Report the malaria status.
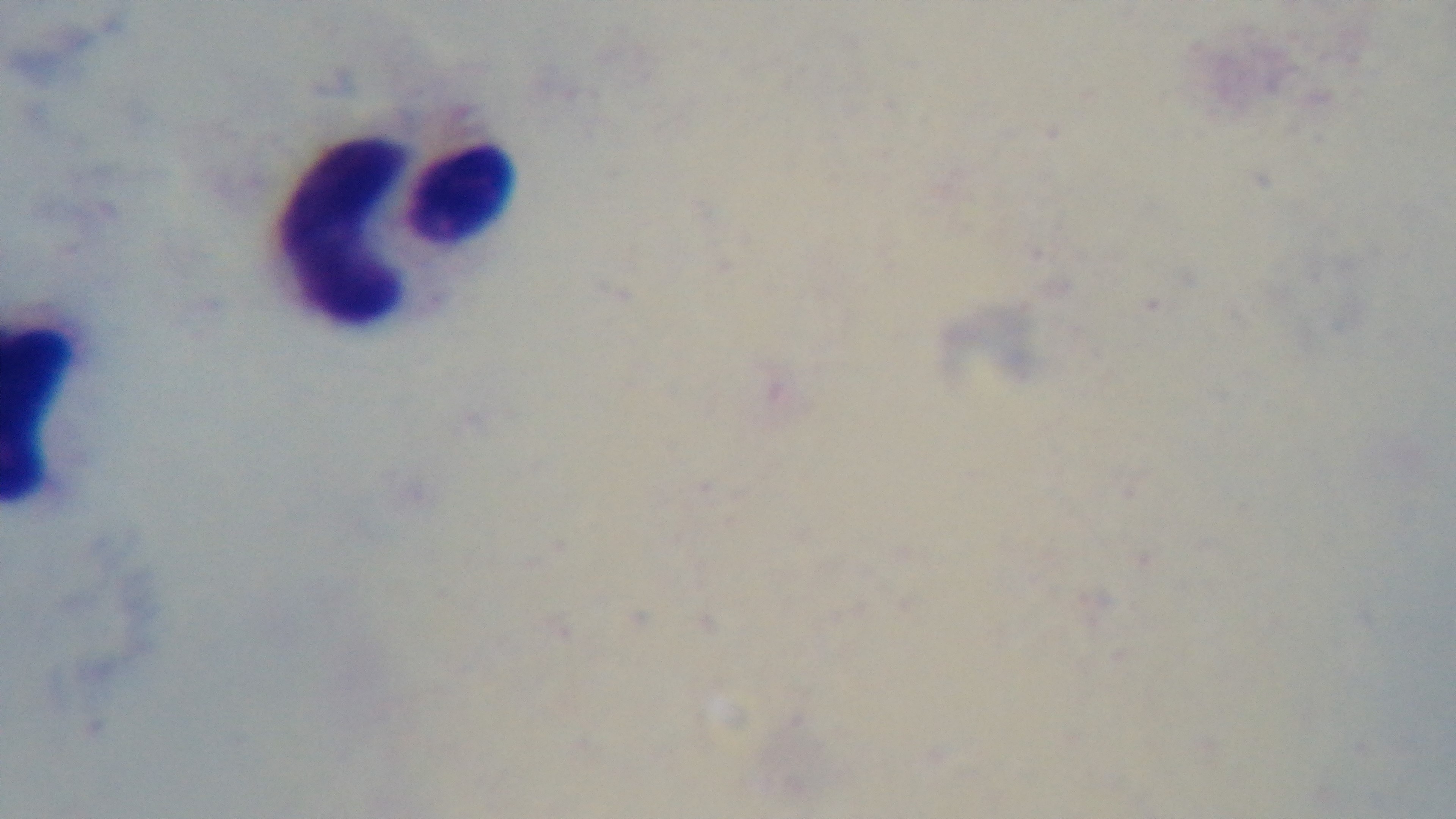
Negative.

Preparation: thick. Giemsa-stained. Single field of view. Mounted 4K digital camera. Oil-immersion objective, 100x. Light microscopy.